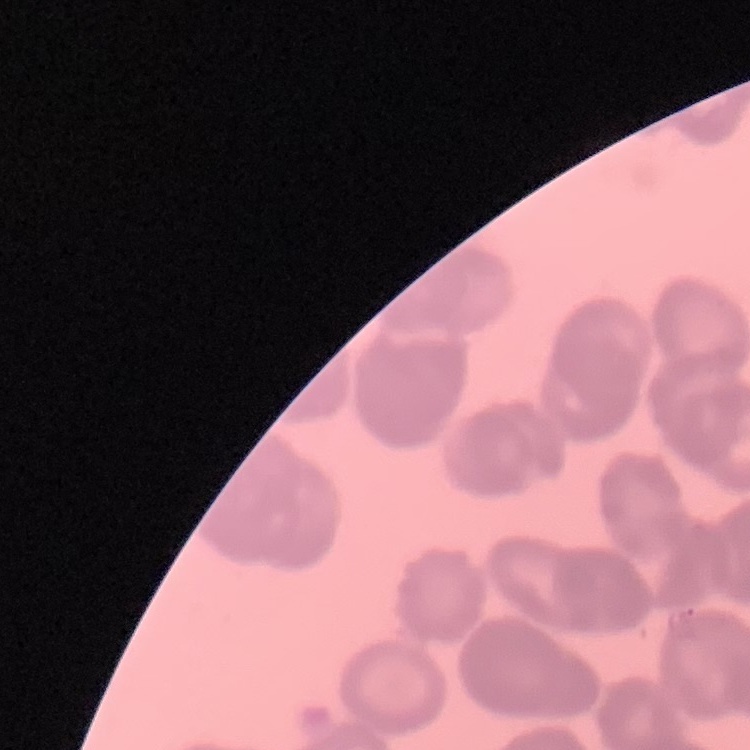

Summary:
  - Red blood cell morphology: rouleaux formation
  - Stain: Field's or Giemsa
  - Preparation: thin blood film
  - Image type: square crop of a larger photomicrograph